Report the malaria status of this cell.
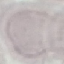
It is uninfected.

Thin blood film. Giemsa-stained preparation. Automatically extracted cell patch, resized to 64 × 64 pixels. Photographed with a smartphone camera at the microscope eyepiece.